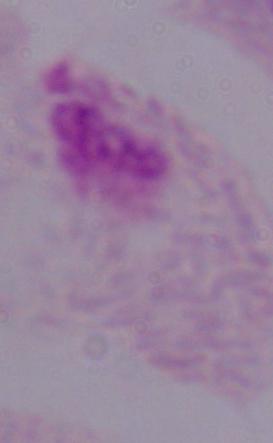 Captured at 1000x magnification. A trichomonad is seen. Photomicrograph.